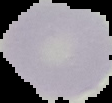

Summary:
  - Result: no Plasmodium parasites detected
  - Image size: 112×103 pixels
  - Preparation: thin blood film
  - Image type: segmented cell region with the area outside set to black